State which cell type is depicted.
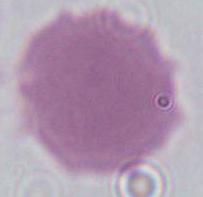
This is an erythrocyte.

Photomicrograph. 1000x magnification.